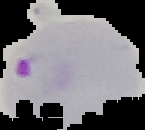

malaria_status: parasitized
image_type: segmented cell region with the area outside set to black
image_size: 145×130 pixels
preparation: thin blood film